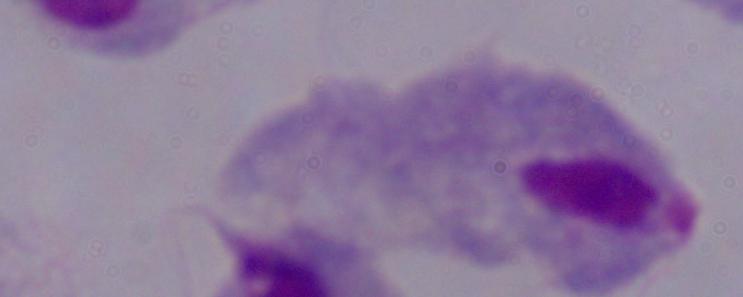
Summary:
  - Modality: micrograph
  - Identification: trichomonad
  - Magnification: 1000x